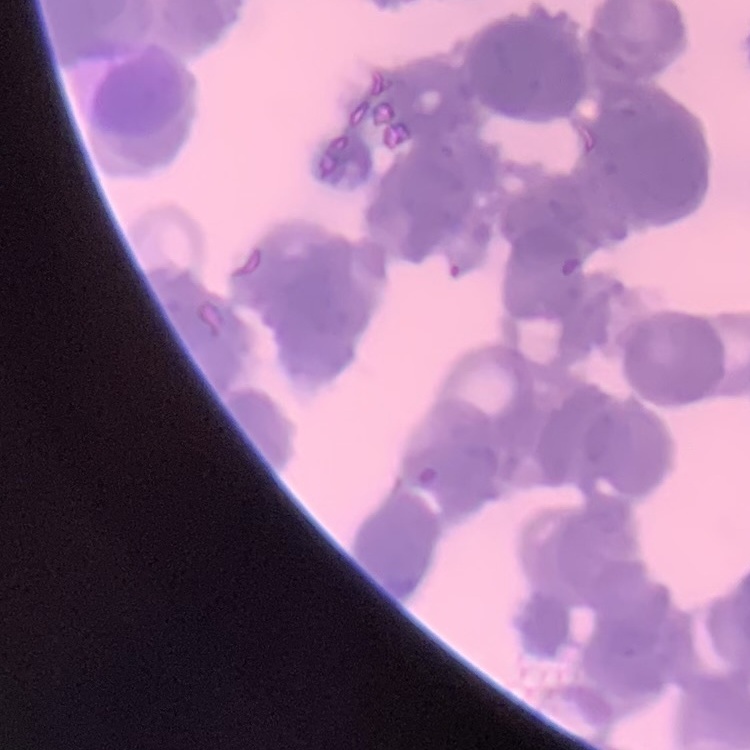

Summary:
  - Erythrocyte morphology: rouleaux formation
  - Image type: one tile cut from a larger photomicrograph
  - Preparation: thin blood smear
  - Stain: Field's or Giemsa